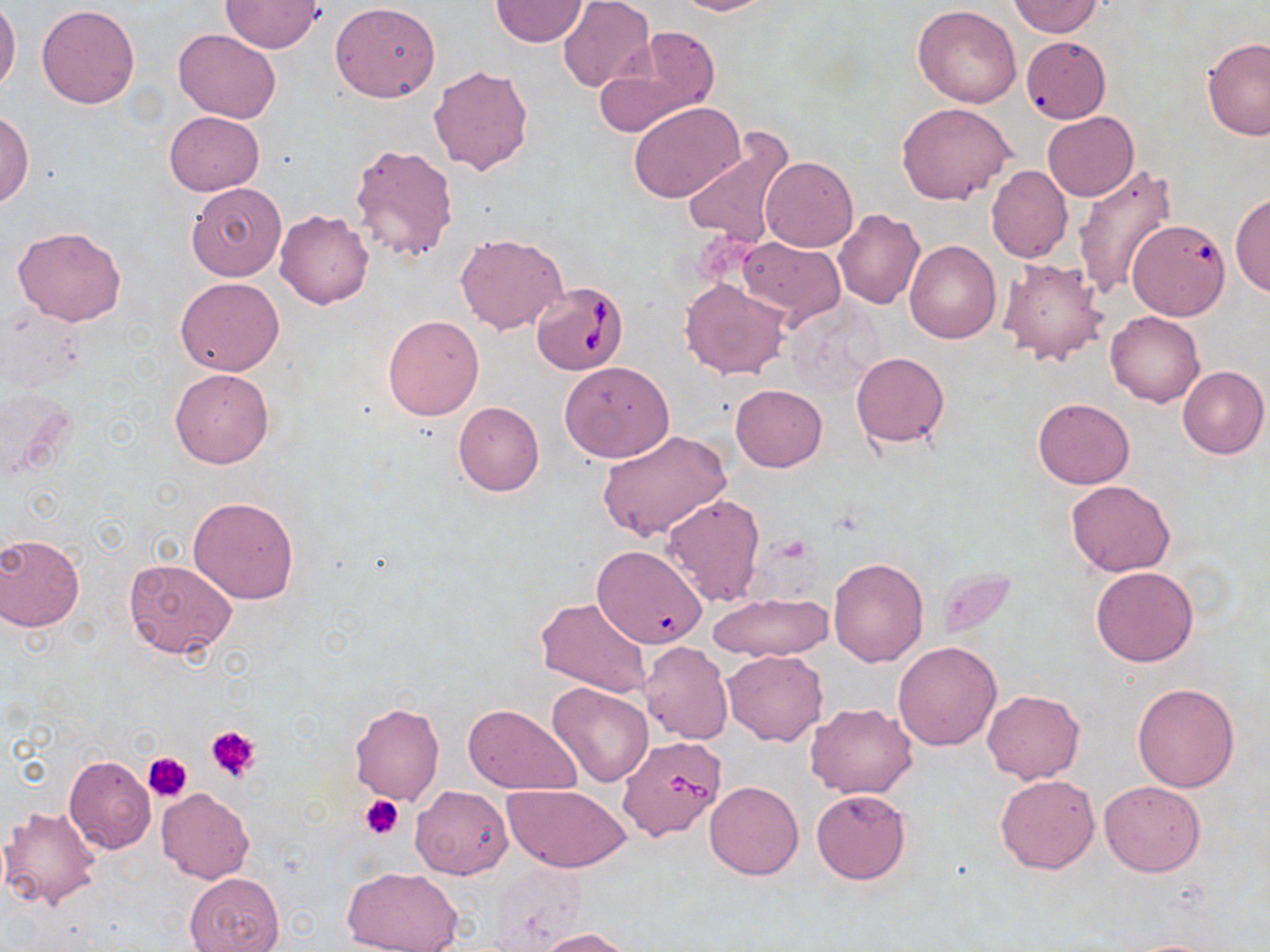
{
  "slide_level_diagnosis": "Babesia divergens",
  "field_of_view": "single",
  "magnification": "1000x",
  "uninfected_red_blood_cell_locations": "approximate bounding boxes as (x1, y1, x2, y2) in pixels: (669, 0, 776, 16), (220, 1, 325, 52), (489, 1, 587, 47), (557, 1, 655, 93), (1006, 1, 1105, 38), (330, 2, 441, 102), (0, 3, 21, 93), (36, 4, 140, 109), (913, 6, 1020, 107), (592, 27, 722, 134), (174, 29, 280, 122), (1022, 36, 1111, 123), (1201, 37, 1270, 140), (429, 63, 536, 177), (897, 102, 1016, 206), (628, 103, 745, 203), (0, 111, 34, 207), (165, 112, 265, 195), (1042, 112, 1139, 200), (680, 126, 797, 251), (348, 142, 458, 263), (761, 156, 858, 251), (986, 165, 1072, 263), (1069, 165, 1177, 299), (185, 181, 286, 281), (1232, 193, 1270, 299), (275, 208, 374, 309), (833, 208, 925, 309), (1127, 220, 1230, 326), (12, 226, 127, 327), (455, 233, 568, 335), (737, 236, 846, 327), (906, 240, 1001, 343), (996, 256, 1110, 367), (175, 277, 285, 377), (680, 278, 791, 380), (1106, 310, 1204, 407), (383, 314, 484, 420), (851, 352, 949, 447), (559, 361, 675, 462), (1177, 366, 1269, 459), (170, 368, 275, 468), (731, 383, 827, 471), (2, 387, 77, 481), (1034, 398, 1134, 488), (452, 401, 545, 496), (595, 428, 732, 543), (1065, 481, 1175, 575), (660, 493, 766, 607), (188, 496, 301, 604), (0, 533, 86, 631), (591, 544, 707, 648), (827, 557, 928, 667), (124, 558, 238, 660), (1090, 565, 1198, 666), (707, 591, 832, 663), (535, 596, 653, 698), (639, 641, 733, 745), (893, 641, 1002, 750), (722, 649, 828, 746), (1133, 682, 1239, 792), (546, 683, 652, 787), (982, 688, 1084, 784), (806, 701, 917, 799), (349, 703, 445, 806), (463, 704, 583, 795), (63, 755, 156, 855), (995, 774, 1099, 873), (704, 779, 804, 880), (1099, 779, 1206, 877), (500, 783, 632, 872), (410, 785, 513, 879), (156, 788, 255, 884), (811, 789, 911, 884), (1, 804, 103, 910), (489, 863, 588, 949), (341, 867, 465, 952), (184, 872, 284, 952), (531, 927, 637, 951), (1118, 938, 1226, 951)",
  "babesia_divergens_infected_red_blood_cell_locations": "approximate bounding boxes as (x1, y1, x2, y2) in pixels: (532, 282, 628, 374), (617, 736, 731, 841)",
  "platelet_locations": "approximate bounding boxes as (x1, y1, x2, y2) in pixels: (205, 724, 260, 784), (143, 750, 193, 801), (361, 794, 404, 840)",
  "image_size": "1270×952 pixels",
  "stain": "May-Grünwald-Giemsa",
  "preparation": "thin blood smear",
  "modality": "optical microscopy"
}